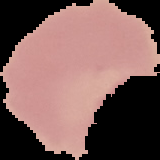
image size = 160×160 pixels
malaria status = uninfected
image type = segmented cell region with the area outside set to black
preparation = thin blood film